Assess this cell for malaria.
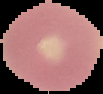

It is uninfected.

From a thin blood film. The area outside the segmented cell region is set to black. Image is 103×94 pixels.